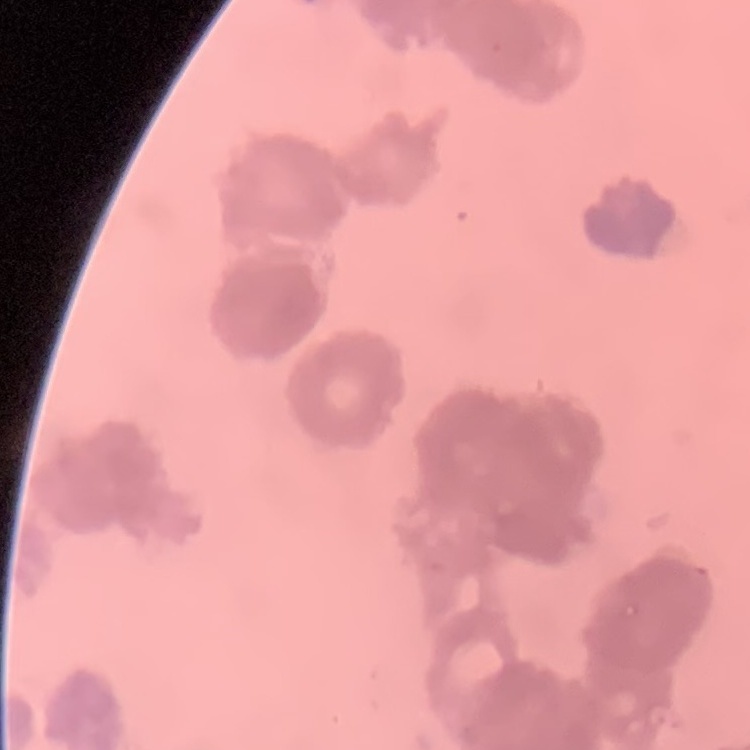
The erythrocytes exhibit rouleaux formation. Square crop of a larger photomicrograph. Field's or Giemsa stain. Thin blood film.